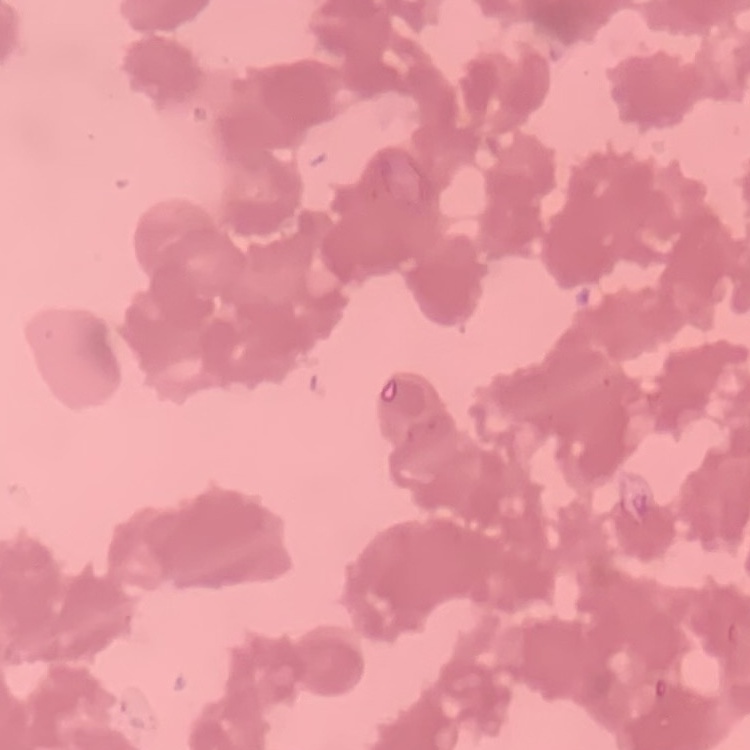
The red blood cells exhibit rouleaux formation. Field's or Giemsa stain. Thin peripheral smear. Square crop of a larger photomicrograph.